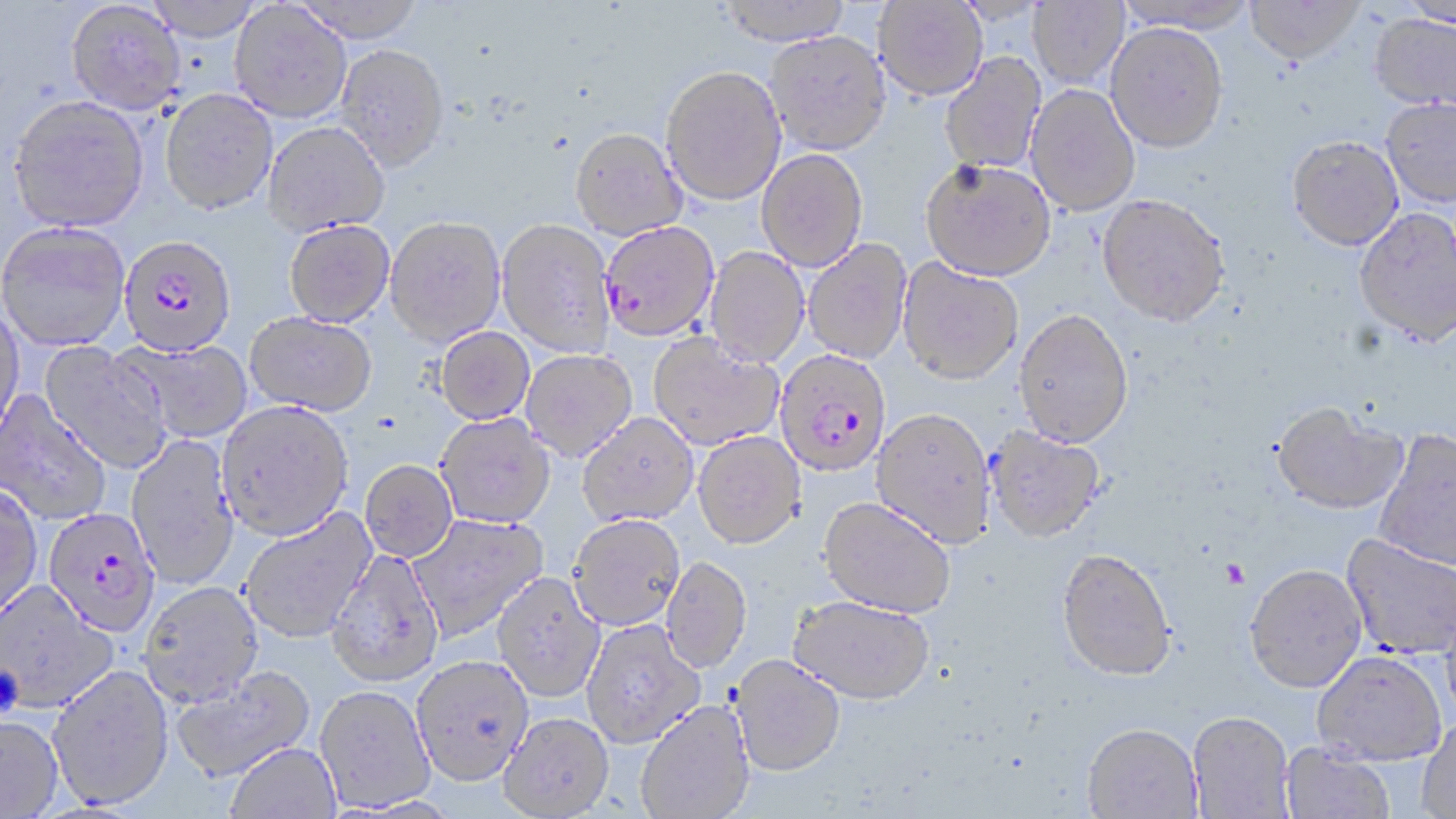 Approximate bounding boxes as (x1,y1)-(x2,y2) corner pairs in pixels. Uninfected red blood cell locations: (290,0)-(427,44), (716,0)-(854,45), (873,0)-(987,100), (1114,0)-(1259,33), (1245,0)-(1365,64), (1028,1)-(1129,87), (66,2)-(186,117), (229,2)-(351,124), (1400,3)-(1456,29), (1370,13)-(1456,111), (1105,22)-(1228,152), (764,31)-(891,155), (337,44)-(450,173), (939,52)-(1046,174), (660,65)-(787,206), (1025,84)-(1141,216), (159,90)-(278,218), (1381,97)-(1456,207), (7,98)-(150,236), (264,122)-(389,238), (570,128)-(688,241), (1287,135)-(1403,250), (756,149)-(868,272), (921,158)-(1056,281), (1096,193)-(1230,326), (1354,207)-(1456,345), (384,218)-(506,347), (496,219)-(616,357), (283,221)-(395,329), (0,224)-(131,354), (803,239)-(912,364), (704,247)-(810,368), (898,258)-(1023,385), (0,302)-(25,444), (1014,308)-(1134,448), (244,313)-(377,418), (435,327)-(535,426), (648,333)-(783,451), (127,339)-(253,443), (38,342)-(171,474), (521,350)-(637,462), (0,391)-(111,525), (1271,402)-(1407,515), (217,404)-(353,543), (870,409)-(997,548), (577,413)-(699,527), (435,414)-(556,530), (984,426)-(1107,544), (1373,428)-(1456,571), (692,432)-(806,550), (125,434)-(240,590), (359,461)-(458,564), (0,484)-(43,622), (818,497)-(956,619), (239,508)-(377,644), (408,513)-(549,642), (567,516)-(685,632), (1341,533)-(1456,659), (1055,548)-(1176,681), (325,551)-(445,689), (661,558)-(752,674), (1244,564)-(1367,693), (492,573)-(606,704), (0,583)-(119,715), (139,583)-(264,710), (788,596)-(935,706), (581,621)-(705,749), (1312,651)-(1446,766), (729,655)-(846,778), (411,657)-(534,789), (47,666)-(174,811), (171,666)-(317,783), (314,687)-(435,813), (635,700)-(756,819), (1188,712)-(1295,818), (498,713)-(614,818), (0,717)-(63,819), (1416,718)-(1456,819), (1082,725)-(1203,819), (1281,742)-(1396,819), (225,744)-(342,819). Plasmodium falciparum-infected red blood cell locations: (601,221)-(720,341), (117,236)-(236,359), (774,349)-(892,478), (42,510)-(160,639). Platelet locations: (1218,558)-(1249,589), (0,665)-(24,717). Slide-level diagnosis: Plasmodium falciparum. One field of a larger specimen. May-Grünwald-Giemsa-stained preparation. Thin blood smear. Captured at 1000x magnification. Image is 1456×819 pixels. Light microscopy.